Name the cell type shown.
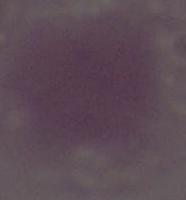

An erythrocyte.

magnification = 1000x
modality = micrograph